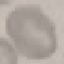 Result: no malaria parasites seen. Thin blood film. Cell patch, automatically extracted from a larger field of view and resized to 64 × 64 pixels. Giemsa-stained preparation. Photographed with a smartphone camera at the microscope eyepiece.